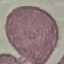

Malaria status: uninfected. Giemsa-stained preparation. Acquired by smartphone through the microscope eyepiece. Thin smear of blood. Automatically extracted cell patch, resized to 64 × 64 pixels.